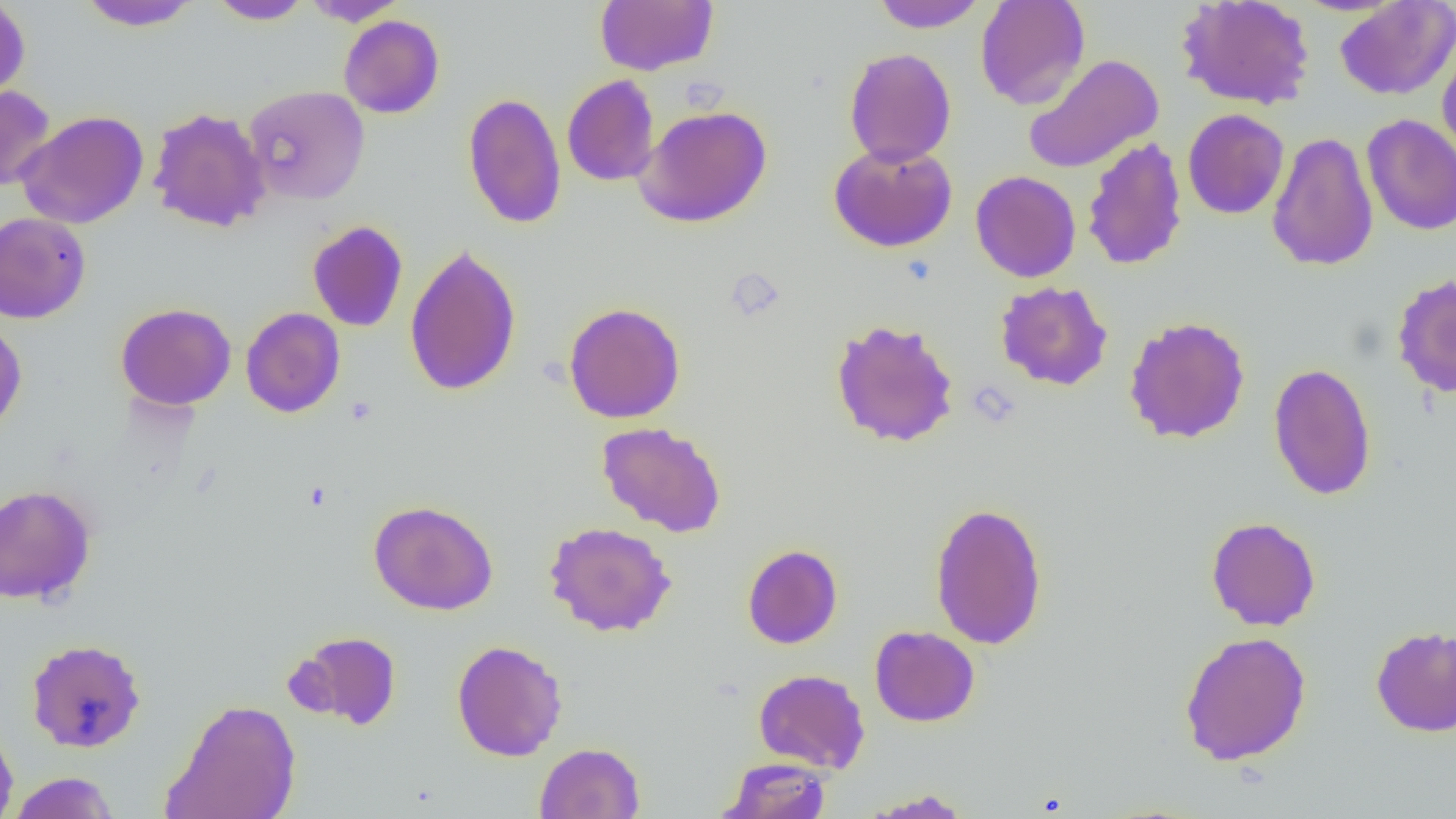
slide-level diagnosis = negative for blood parasites
field of view = single
uninfected red blood cell locations = approximate bounding boxes as (x1,y1)-(x2,y2) corner pairs in pixels: (0,0)-(30,101), (207,0)-(314,25), (301,0)-(409,26), (595,0)-(718,75), (975,0)-(1091,110), (1176,0)-(1315,111), (76,1)-(200,31), (871,1)-(987,33), (1335,1)-(1456,100), (338,15)-(445,119), (1437,36)-(1456,165), (843,47)-(957,167), (1022,54)-(1164,174), (562,74)-(659,186), (0,84)-(56,191), (243,85)-(371,206), (463,91)-(566,229), (635,105)-(773,228), (148,106)-(271,232), (1182,109)-(1289,219), (15,111)-(149,229), (1361,114)-(1456,235), (1267,132)-(1379,272), (1082,136)-(1188,271), (828,142)-(957,252), (970,170)-(1081,282), (0,212)-(91,324), (307,220)-(408,332), (404,243)-(522,397), (1391,273)-(1456,398), (995,281)-(1113,391), (115,302)-(237,410), (563,302)-(686,423), (240,307)-(345,417), (1123,316)-(1251,444), (830,318)-(960,448), (0,320)-(27,438), (1267,362)-(1377,501), (596,421)-(727,538), (0,484)-(97,605), (368,500)-(499,615), (929,502)-(1048,650), (1206,517)-(1321,630), (544,521)-(676,637), (742,543)-(843,649), (869,625)-(980,727), (1370,625)-(1456,738), (289,630)-(403,731), (1178,631)-(1311,766), (25,638)-(147,753), (451,639)-(567,761), (753,668)-(870,773), (162,698)-(302,819), (0,721)-(19,819), (534,742)-(645,818), (719,757)-(833,819), (7,772)-(121,818), (861,788)-(975,818)
preparation = thin blood smear
magnification = 1000x
image size = 1456×819 pixels
modality = optical microscopy